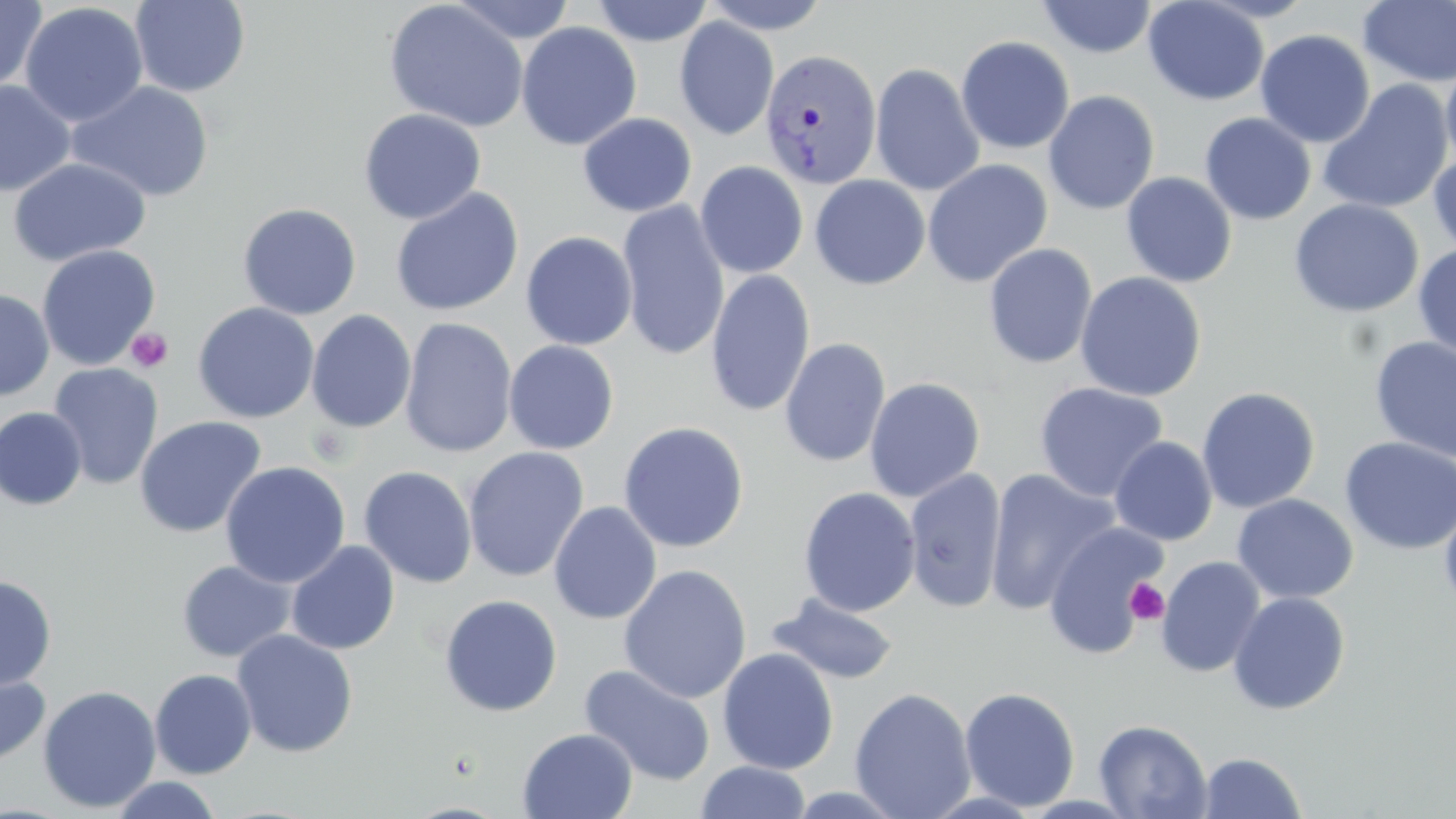

slide-level diagnosis = Plasmodium vivax
image size = 1456×819 pixels
uninfected red blood cell locations = approximate bounding boxes as (x1,y1)-(x2,y2) corner pairs in pixels: (0,0)-(46,94), (129,0)-(251,97), (383,0)-(530,133), (448,0)-(578,44), (591,0)-(713,46), (699,0)-(832,34), (1037,0)-(1158,58), (1142,0)-(1270,106), (1357,0)-(1456,88), (20,2)-(149,128), (674,17)-(779,141), (516,21)-(642,150), (1255,28)-(1376,148), (955,36)-(1075,154), (1440,58)-(1456,172), (870,63)-(985,196), (0,80)-(76,197), (66,80)-(215,202), (1317,81)-(1453,215), (1043,90)-(1160,215), (358,108)-(486,225), (578,112)-(696,217), (1199,113)-(1317,225), (1428,149)-(1456,259), (7,157)-(151,267), (922,159)-(1053,287), (695,161)-(808,279), (1121,172)-(1237,288), (809,175)-(931,289), (390,187)-(524,317), (1289,198)-(1424,317), (617,200)-(730,361), (237,202)-(362,320), (520,231)-(638,350), (983,242)-(1097,369), (36,244)-(161,371), (1413,244)-(1456,360), (705,269)-(816,418), (1075,271)-(1206,401), (0,288)-(54,401), (192,302)-(319,424), (306,309)-(417,433), (399,317)-(518,458), (1369,334)-(1456,464), (779,338)-(890,468), (503,340)-(619,454), (48,363)-(163,489), (864,377)-(985,502), (1034,382)-(1168,503), (1196,387)-(1320,513), (0,407)-(87,510), (134,416)-(266,538), (618,421)-(749,553), (1110,436)-(1218,545), (1339,437)-(1456,555), (463,447)-(589,583), (220,461)-(351,588), (358,466)-(477,589), (904,467)-(1006,613), (985,468)-(1120,615), (798,487)-(921,617), (1232,494)-(1358,604), (1439,495)-(1456,614), (548,501)-(662,624), (1044,521)-(1166,657), (286,540)-(400,655), (1155,555)-(1266,678), (176,559)-(296,663), (618,564)-(752,704), (0,575)-(57,691), (1228,591)-(1350,715), (766,593)-(900,686), (439,594)-(563,717), (231,629)-(358,758), (716,648)-(840,775), (579,663)-(717,786), (0,665)-(51,770), (149,668)-(257,779), (37,685)-(161,813), (959,686)-(1080,811), (849,687)-(976,818), (1093,718)-(1213,818), (517,728)-(638,818), (1197,751)-(1307,818), (696,760)-(811,818), (108,776)-(224,818), (779,784)-(913,818)
Plasmodium vivax-infected red blood cell locations = approximate bounding boxes as (x1,y1)-(x2,y2) corner pairs in pixels: (760,49)-(881,190)
field of view = one of a larger specimen
stain = May-Grünwald-Giemsa
platelet locations = approximate bounding boxes as (x1,y1)-(x2,y2) corner pairs in pixels: (126,328)-(173,373), (1124,579)-(1170,625)
modality = optical microscopy
preparation = thin blood smear
magnification = 1000x